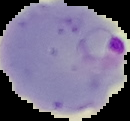
image size = 130×121 pixels
image type = segmented cell region with the area outside set to black
preparation = thin blood film
malaria status = parasitized